Locate every Plasmodium parasite.
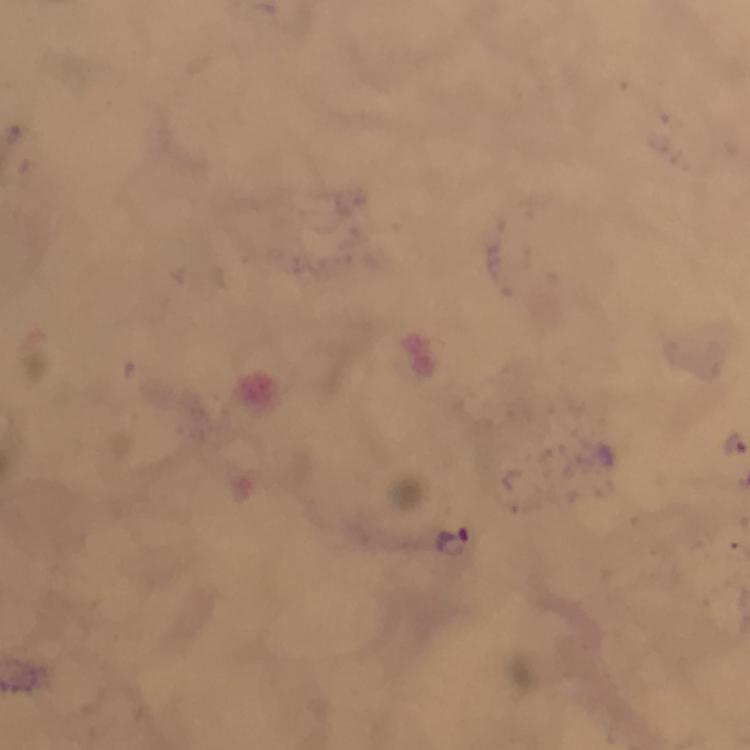
Approximate centers as (x, y) in pixels.
Plasmodium parasites: (736, 444), (453, 541).

preparation = thick smear
image size = 750×750 pixels
context = from a malaria diagnostic workup
cropped from = a single field of view
immersion oil = applied
capture = smartphone photograph through a microscope
stain = Giemsa
magnification = 100x